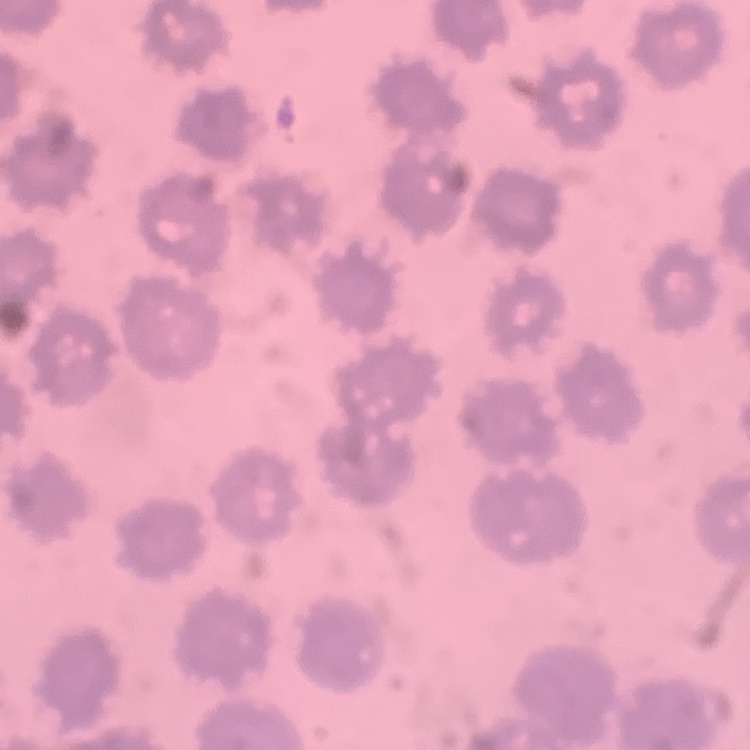

Summary:
  - Red blood cell morphology: no rouleaux formation
  - Stain: Field's or Giemsa
  - Preparation: thin peripheral smear
  - Image type: square crop of a larger photomicrograph